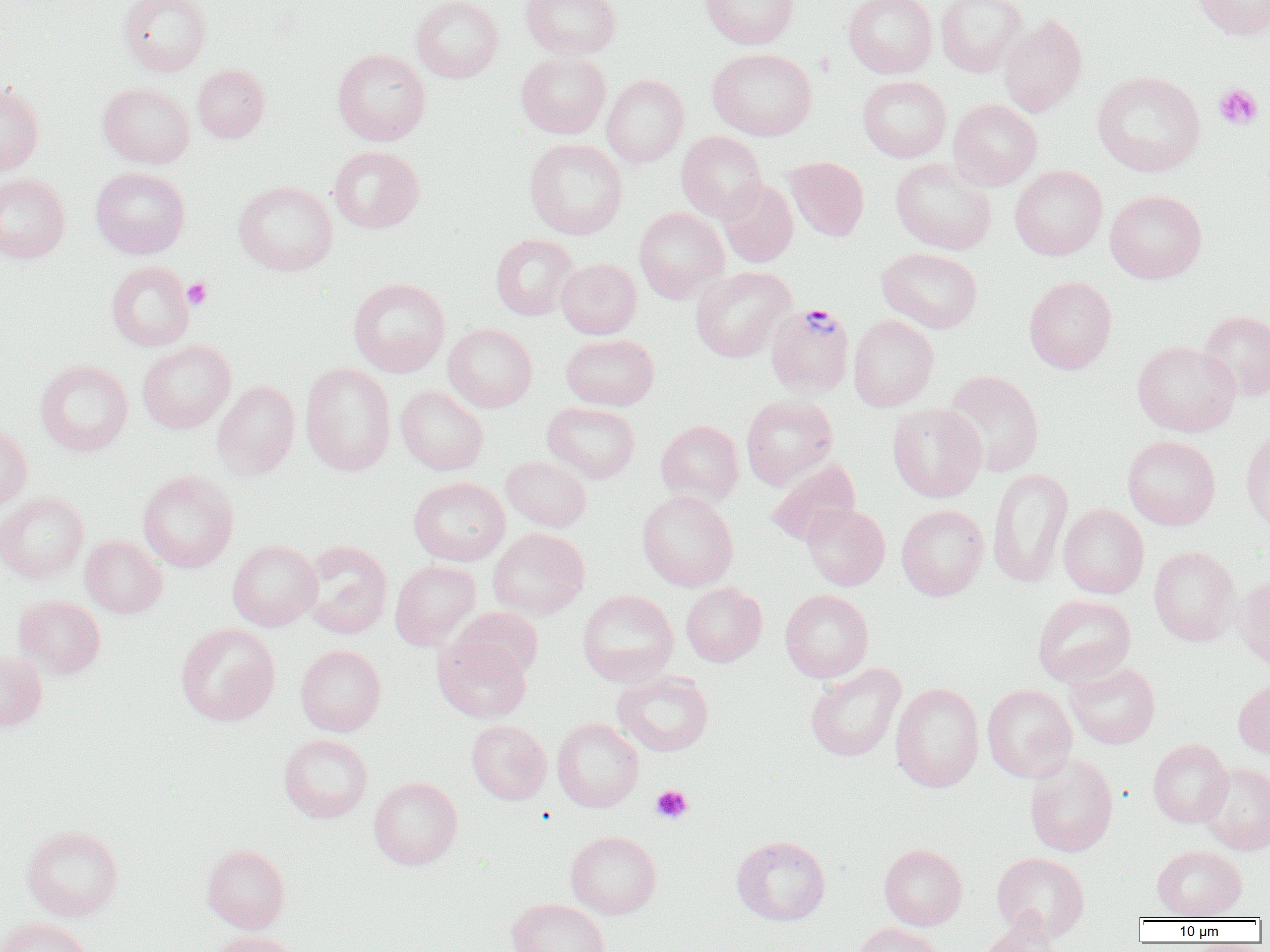
Summary:
  - Coordinate format: approximate bounding boxes as (x1, y1, x2, y2) in pixels
  - Plasmodium vivax-infected red blood cell locations: (765, 302, 856, 398)
  - Uninfected red blood cell locations: (118, 0, 211, 76), (411, 0, 503, 82), (521, 0, 621, 60), (700, 0, 798, 49), (843, 0, 937, 78), (936, 0, 1027, 77), (1192, 0, 1270, 40), (999, 15, 1087, 117), (332, 48, 431, 145), (708, 48, 817, 140), (516, 51, 611, 138), (192, 64, 269, 143), (1092, 71, 1206, 176), (601, 74, 689, 167), (857, 76, 951, 162), (0, 82, 44, 176), (98, 83, 195, 168), (948, 99, 1042, 190), (676, 131, 767, 222), (524, 138, 627, 239), (329, 146, 425, 233), (785, 157, 869, 241), (890, 157, 997, 255), (1010, 165, 1107, 260), (90, 167, 189, 258), (0, 173, 71, 263), (717, 178, 798, 267), (233, 181, 337, 275), (1105, 189, 1206, 283), (634, 207, 729, 303), (490, 234, 579, 320), (876, 247, 983, 333), (557, 259, 641, 339), (106, 261, 195, 351), (691, 267, 795, 362), (1024, 276, 1117, 374), (348, 278, 449, 376), (1197, 310, 1270, 401), (848, 315, 939, 411), (443, 323, 537, 412), (561, 333, 659, 410), (137, 340, 235, 433), (1132, 341, 1241, 436), (35, 360, 133, 456), (300, 363, 396, 476), (943, 370, 1045, 477), (212, 380, 300, 480), (395, 386, 488, 475), (741, 394, 838, 489), (542, 402, 640, 484), (887, 402, 987, 502), (656, 420, 744, 506), (1241, 424, 1270, 533), (0, 427, 32, 512), (1122, 435, 1220, 530), (501, 456, 591, 532), (766, 458, 860, 547), (987, 468, 1073, 588), (137, 470, 238, 572), (408, 476, 510, 566), (637, 490, 738, 591), (0, 492, 89, 583), (801, 503, 890, 590), (1058, 504, 1149, 598), (896, 505, 988, 600), (488, 528, 589, 620), (80, 535, 167, 618), (227, 540, 322, 631), (300, 540, 393, 638), (1148, 545, 1241, 646), (390, 560, 481, 650), (1236, 573, 1270, 670), (681, 582, 767, 667), (577, 589, 678, 686), (779, 589, 873, 682), (1032, 594, 1136, 687), (13, 595, 106, 679), (451, 606, 543, 681), (175, 623, 280, 726), (433, 636, 532, 723), (295, 644, 386, 736), (0, 650, 46, 731), (1065, 661, 1160, 749), (805, 663, 905, 762), (613, 671, 714, 757), (1234, 675, 1270, 759), (891, 682, 984, 792), (982, 684, 1077, 782), (552, 718, 643, 812), (466, 720, 551, 804), (278, 734, 373, 823), (1148, 738, 1232, 827), (1024, 754, 1118, 857), (1199, 763, 1270, 855), (369, 776, 462, 869), (21, 824, 123, 921), (565, 830, 661, 918), (732, 835, 831, 925), (201, 844, 290, 933), (879, 844, 967, 930), (1152, 845, 1247, 920), (992, 852, 1090, 941), (507, 898, 610, 952), (978, 917, 1064, 951), (1, 918, 94, 952), (851, 922, 945, 952), (207, 929, 301, 952)
  - Platelet locations: (1214, 84, 1263, 130), (182, 277, 211, 310), (651, 785, 693, 823)
  - Slide-level diagnosis: Plasmodium vivax
  - Modality: light microscopy
  - Magnification: 1000x
  - Preparation: thin blood film
  - Field of view: single
  - Image size: 1270×952 pixels